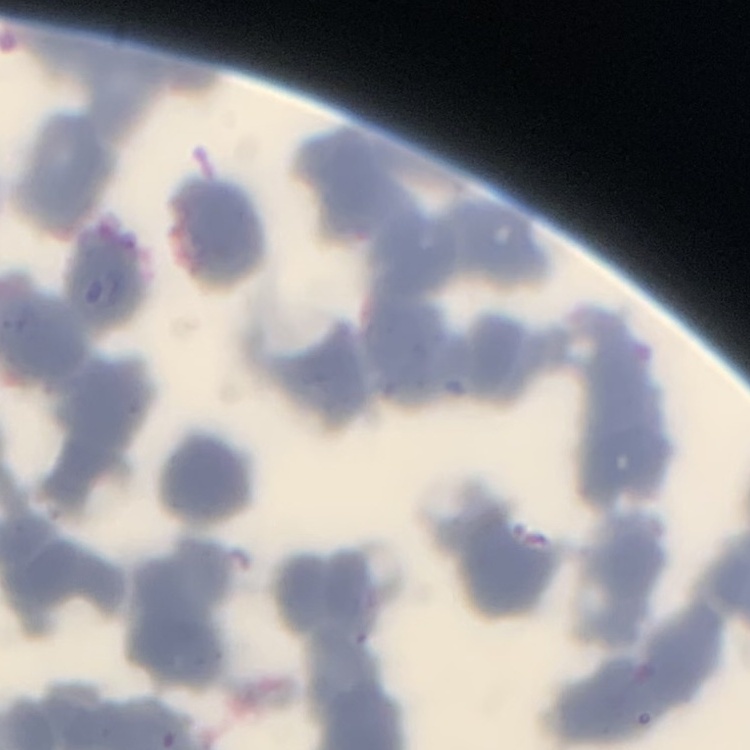
Summary:
  - Erythrocyte morphology: rouleaux formation
  - Stain: Field's or Giemsa
  - Preparation: thin peripheral smear
  - Image type: square crop of a larger photomicrograph